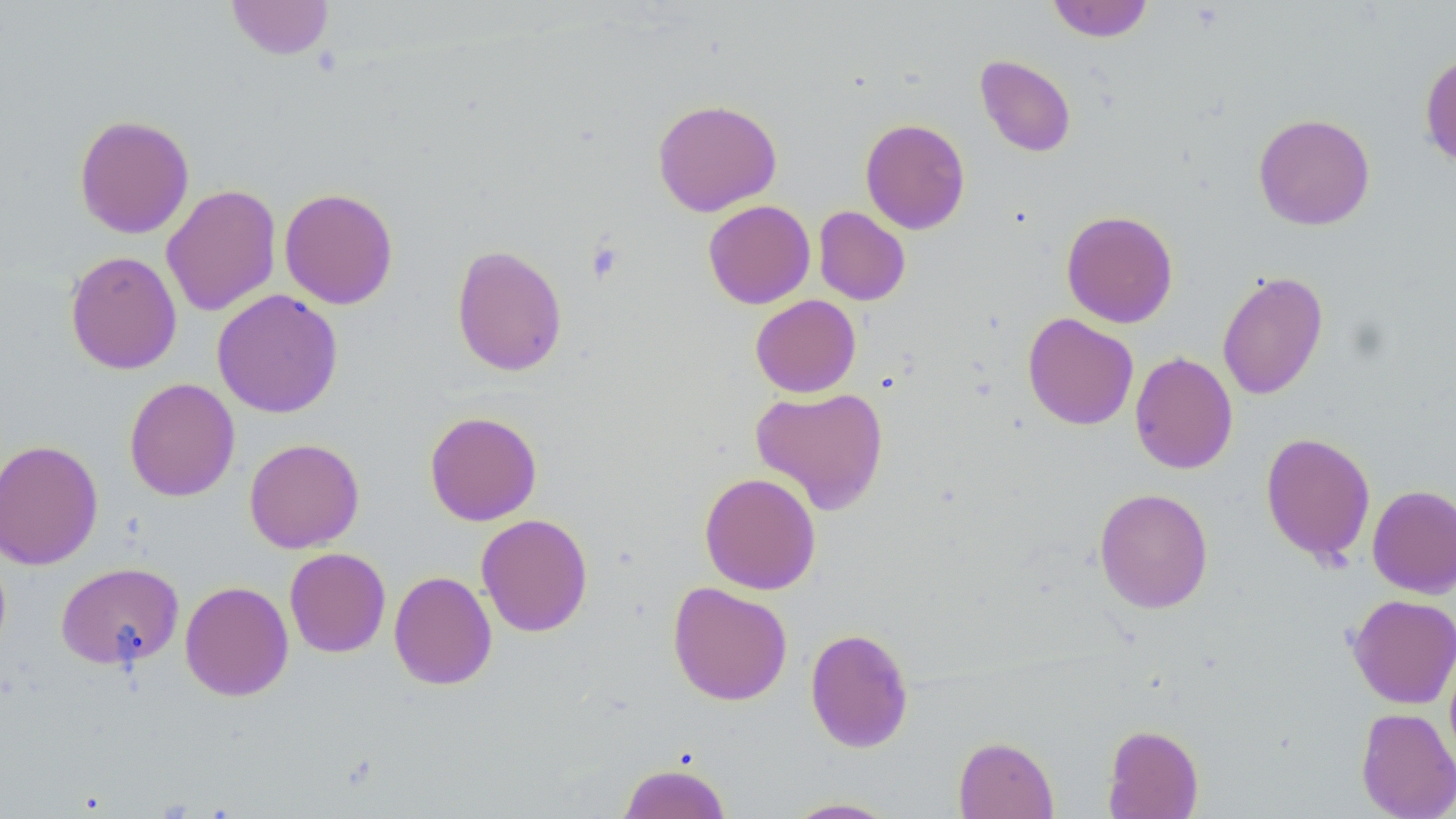

Approximate bounding boxes as (x1, y1, x2, y2) in pixels. Uninfected red blood cell locations: (228, 0, 333, 59), (1046, 0, 1154, 42), (1419, 52, 1456, 168), (975, 54, 1076, 157), (652, 98, 782, 216), (1253, 113, 1375, 230), (74, 114, 194, 239), (860, 118, 970, 234), (161, 184, 281, 316), (279, 187, 398, 309), (703, 200, 815, 309), (813, 206, 911, 306), (1061, 210, 1178, 328), (451, 244, 567, 376), (65, 250, 182, 374), (1217, 270, 1328, 400), (212, 289, 343, 418), (750, 294, 861, 397), (1023, 312, 1139, 430), (1130, 351, 1238, 474), (124, 378, 240, 501), (750, 386, 889, 514), (424, 411, 542, 525), (1260, 431, 1376, 564), (244, 438, 364, 553), (0, 439, 103, 570), (699, 472, 821, 595), (1367, 484, 1456, 598), (1094, 487, 1213, 614), (476, 513, 593, 637), (284, 548, 391, 657), (56, 562, 185, 670), (389, 571, 497, 690), (180, 580, 294, 701), (668, 581, 792, 706), (1347, 594, 1456, 708), (805, 627, 915, 753), (1355, 707, 1456, 819), (1102, 724, 1203, 818), (953, 736, 1058, 818), (617, 761, 732, 819), (783, 797, 900, 818). Platelet locations: (585, 238, 626, 285). Slide-level diagnosis: no evidence of blood parasites. Single field of view. May-Grünwald-Giemsa-stained preparation. Thin blood smear. Image is 1456×819 pixels. Light microscopy. 1000x magnification.